Assess the morphology of the erythrocytes.
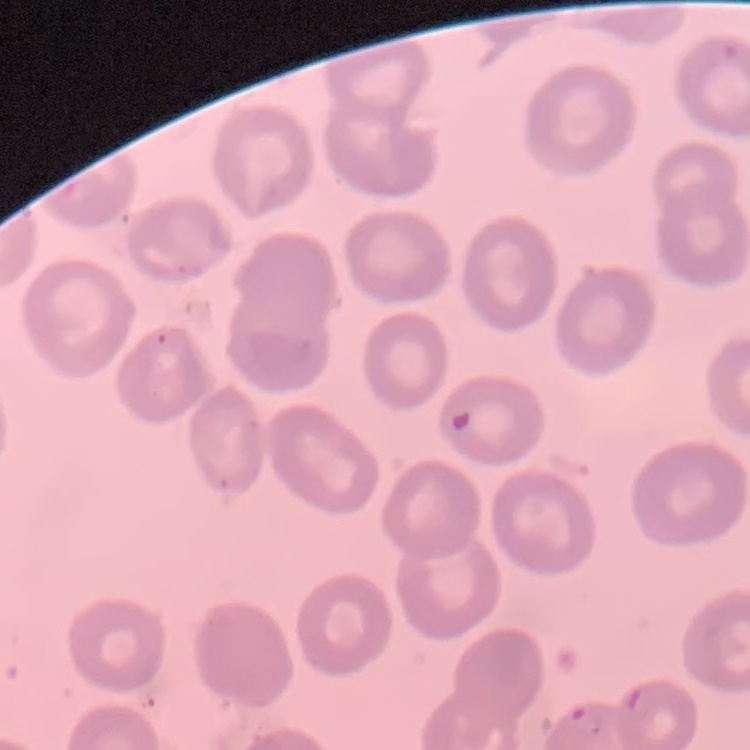
They show no rouleaux formation.

Summary:
  - Image type: square crop of a larger photomicrograph
  - Preparation: thin blood film
  - Stain: Field's or Giemsa